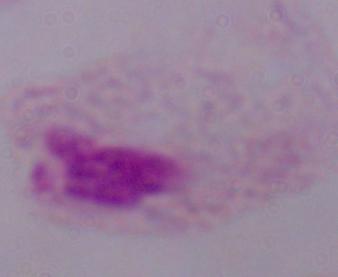

identification = trichomonad
magnification = 1000x
modality = photomicrograph